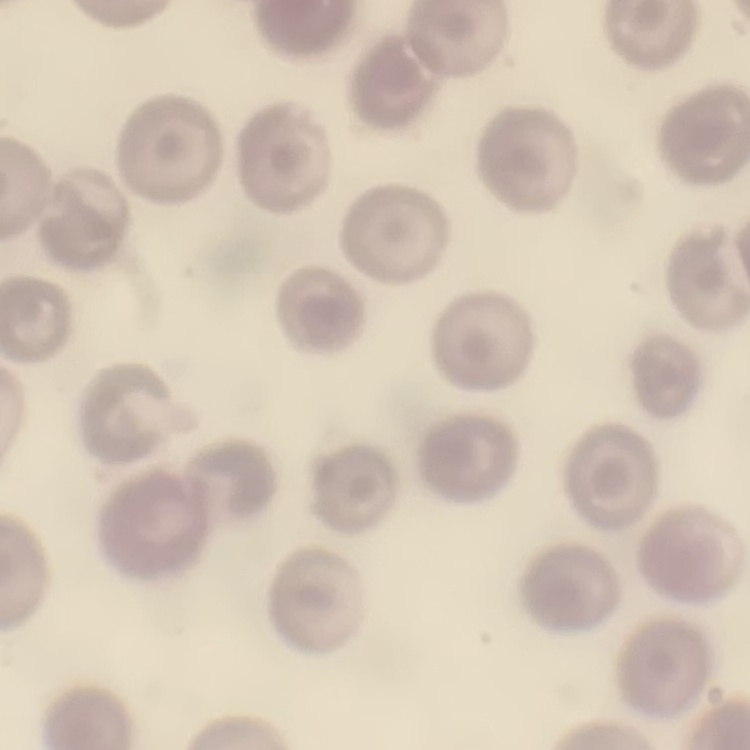
Summary:
  - Red blood cell morphology: no rouleaux formation
  - Image type: square crop of a larger photomicrograph
  - Preparation: thin peripheral smear
  - Stain: Field's or Giemsa